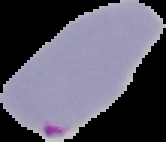

malaria status = parasitized
image size = 166×142 pixels
preparation = thin blood film
image type = segmented cell region on a black background